Assess this cell for malaria.
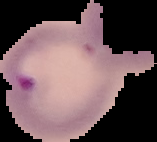
It is parasitized.

Summary:
  - Image size: 157×142 pixels
  - Preparation: thin blood smear
  - Image type: segmented cell region with the area outside set to black